Assess this cell for malaria.
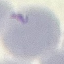

It is uninfected.

stain = Giemsa
preparation = thin smear
capture = smartphone camera at the microscope eyepiece
image type = cell patch, automatically extracted from a larger field of view and resized to 64 × 64 pixels